Outline each Plasmodium ovale-infected red blood cell.
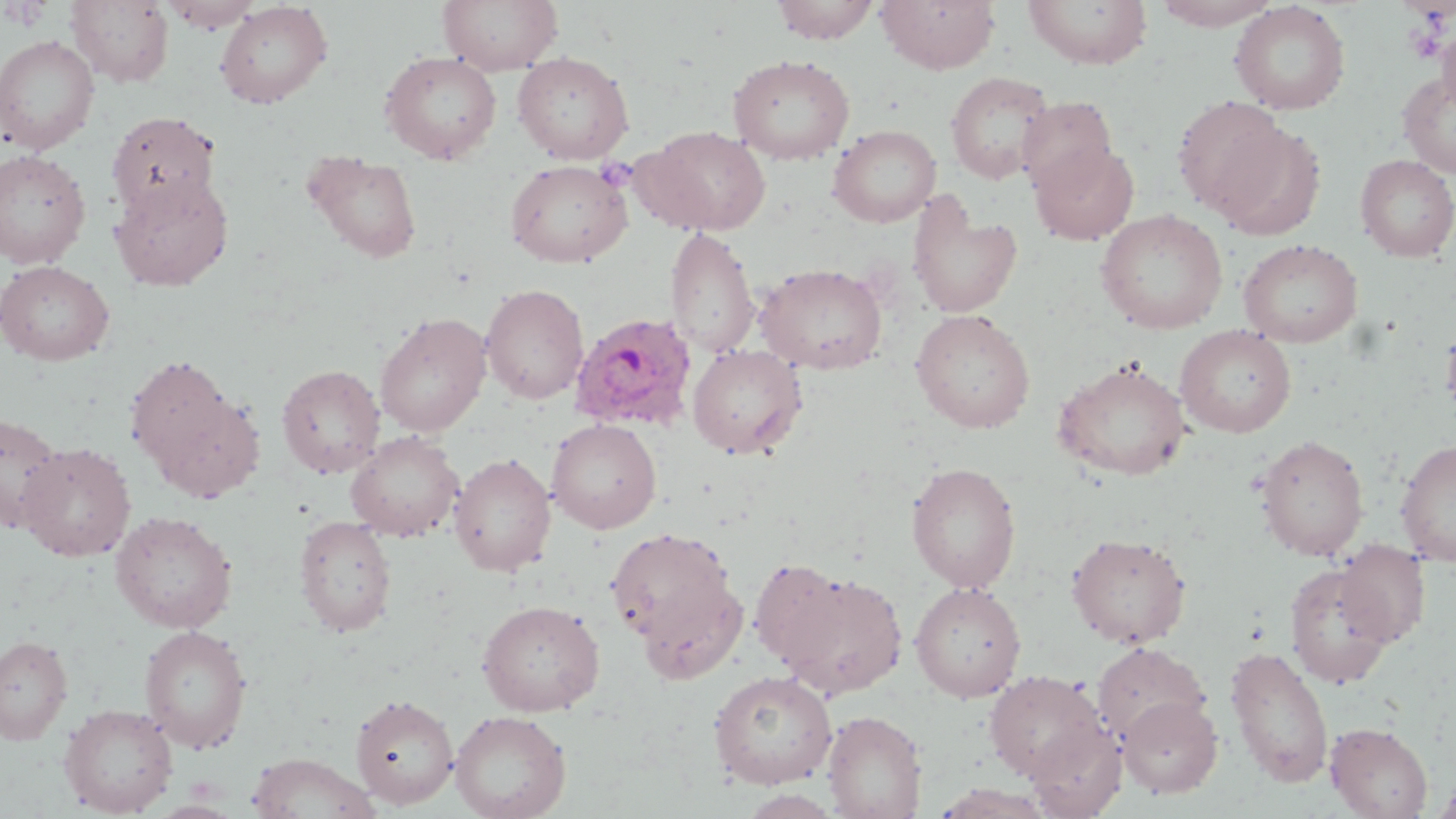
Approximate bounding boxes as (x1,y1)-(x2,y2) corner pairs in pixels.
Plasmodium ovale-infected red blood cells: (569,312)-(698,433).

slide-level diagnosis = Plasmodium ovale
uninfected red blood cell locations (subset) = approximate bounding boxes as (x1,y1)-(x2,y2) corner pairs in pixels: (66,0)-(173,87), (438,0)-(563,76), (771,0)-(881,44), (875,0)-(1000,73), (1022,0)-(1152,69), (1149,0)-(1284,30), (156,1)-(265,32), (215,1)-(333,109), (1229,1)-(1351,115), (1437,23)-(1456,116), (0,35)-(100,154), (379,51)-(502,164), (512,52)-(634,163), (727,54)-(856,164), (1397,69)-(1456,179), (945,71)-(1055,185), (1172,96)-(1289,220), (1016,97)-(1117,196), (106,111)-(221,220), (1213,122)-(1327,242), (828,125)-(941,228), (641,126)-(772,235), (1029,140)-(1139,245), (0,149)-(91,268), (303,150)-(423,263), (1356,154)-(1456,262), (505,159)-(632,267), (110,174)-(233,291), (907,195)-(1023,319), (1095,209)-(1229,334), (665,227)-(759,358), (1238,239)-(1364,347), (0,260)-(115,365), (755,263)-(888,375), (480,283)-(589,404), (911,309)-(1036,433), (374,313)-(492,437), (1440,318)-(1456,427), (1174,325)-(1296,437), (687,344)-(807,459), (125,355)-(235,472), (1053,359)-(1192,481), (276,363)-(385,478), (149,388)-(265,502), (0,410)-(66,534), (547,418)-(662,533), (345,431)-(464,542), (1255,434)-(1369,561), (1395,439)-(1456,566), (19,442)-(136,561), (448,453)-(557,576), (906,461)-(1022,593), (110,511)-(237,633), (295,514)-(397,637), (605,527)-(738,653), (1066,532)-(1192,648), (1335,541)-(1430,647), (749,557)-(852,671), (1284,562)-(1397,688), (634,568)-(748,685), (773,570)-(909,699), (910,582)-(1026,702), (477,599)-(605,716), (139,624)-(253,753), (0,636)-(73,744), (1090,642)-(1210,746), (1225,646)-(1334,788), (708,670)-(838,789), (984,670)-(1106,782), (350,694)-(458,808), (1118,694)-(1222,798), (59,703)-(178,816), (450,710)-(572,819), (823,710)-(928,819), (1025,721)-(1127,818), (1325,722)-(1433,818), (247,752)-(380,819), (1432,777)-(1456,819), (934,783)-(1055,819)
field of view = single
image size = 1456×819 pixels
preparation = thin blood film
stain = May-Grünwald-Giemsa
magnification = 1000x
modality = optical microscopy
platelet locations (subset) = approximate bounding boxes as (x1,y1)-(x2,y2) corner pairs in pixels: (594,157)-(636,192)